State which parasite is depicted.
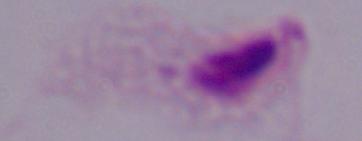
A trichomonad.

modality: micrograph
magnification: 1000x